Name the parasite shown.
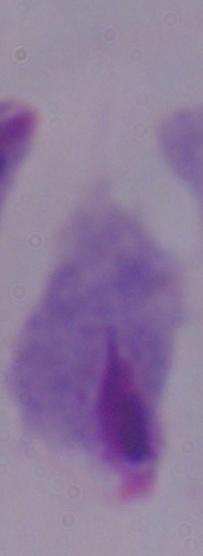
This is a trichomonad.

Summary:
  - Magnification: 1000x
  - Modality: micrograph